Give the extent of all Plasmodium falciparum-infected red blood cells.
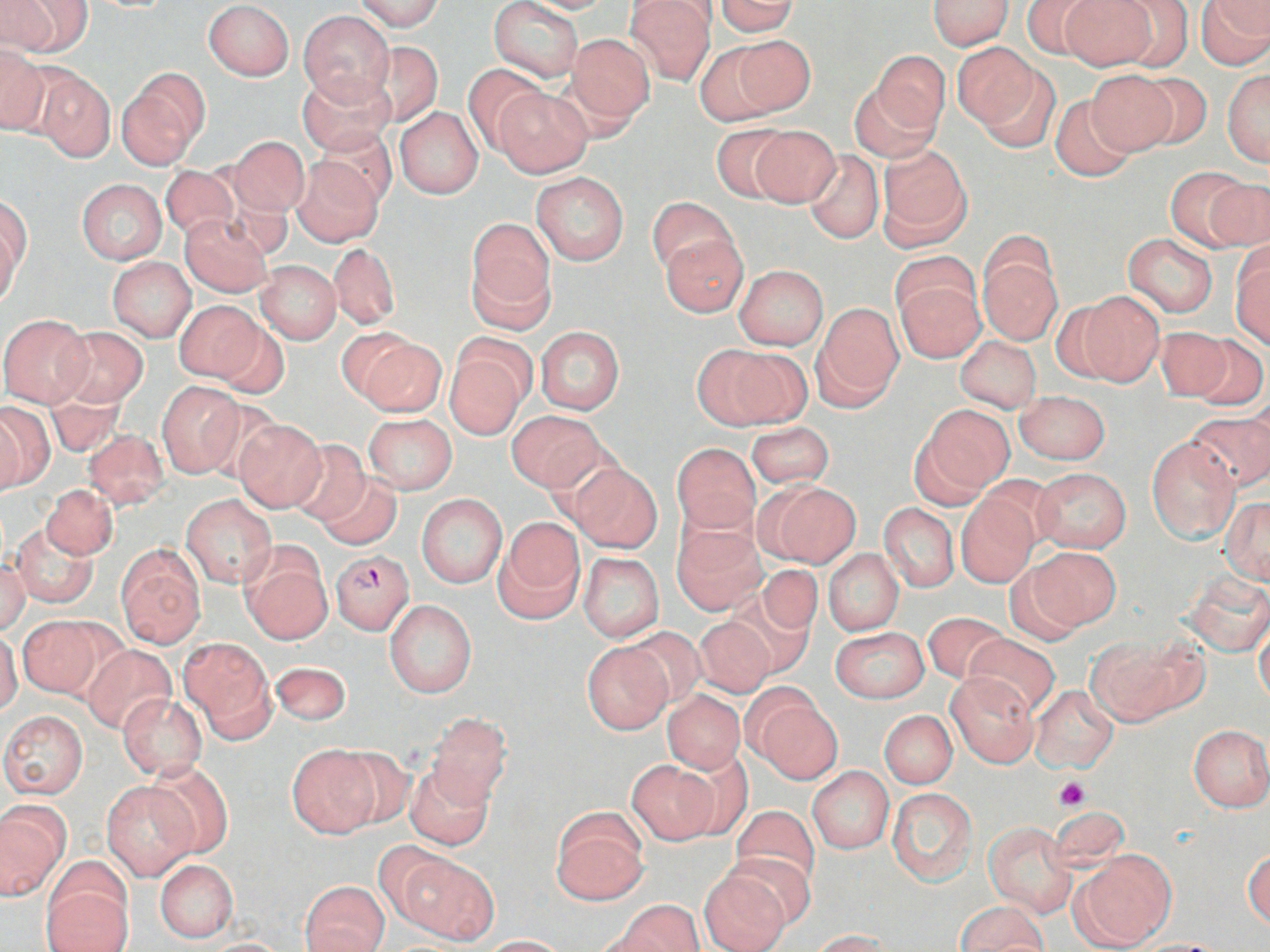
Approximate bounding boxes as (x1,y1)-(x2,y2) corner pairs in pixels.
Plasmodium falciparum-infected red blood cells: (330,551)-(414,634).

Summary:
  - Platelet locations: (1056,776)-(1089,810)
  - Uninfected red blood cell locations: (355,0)-(444,31), (515,0)-(620,15), (625,0)-(715,86), (714,0)-(801,35), (928,0)-(1013,50), (1019,0)-(1106,59), (1058,0)-(1158,71), (1107,0)-(1194,71), (1197,0)-(1270,68), (4,1)-(89,57), (202,1)-(294,79), (489,1)-(583,83), (297,10)-(395,105), (565,33)-(657,128), (727,35)-(816,116), (365,40)-(445,128), (952,42)-(1044,136), (0,44)-(49,135), (696,44)-(784,125), (872,51)-(950,134), (463,63)-(550,152), (977,65)-(1062,153), (34,68)-(114,162), (118,68)-(209,167), (1086,70)-(1178,154), (1223,70)-(1270,167), (298,71)-(397,154), (1132,73)-(1214,150), (852,79)-(941,161), (494,85)-(593,178), (1050,94)-(1138,182), (394,106)-(484,200), (709,123)-(796,200), (747,125)-(841,208), (314,126)-(397,208), (230,136)-(309,216), (876,142)-(972,250), (802,148)-(884,245), (292,157)-(384,246), (160,164)-(239,243), (1165,168)-(1257,251), (532,172)-(629,265), (1206,176)-(1270,251), (76,179)-(167,265), (1,198)-(30,296), (646,198)-(738,278), (180,214)-(274,296), (465,222)-(556,329), (1,226)-(21,309), (1122,233)-(1218,318), (658,234)-(749,316), (327,242)-(399,329), (1231,243)-(1270,347), (890,250)-(978,329), (978,250)-(1062,344), (107,257)-(196,341), (255,261)-(341,344), (734,265)-(828,350), (895,276)-(986,363), (1074,290)-(1165,387), (173,300)-(267,384), (812,303)-(904,409), (0,313)-(93,406), (208,318)-(290,400), (534,325)-(625,415), (57,326)-(148,407), (1154,326)-(1236,400), (353,332)-(446,417), (1190,333)-(1269,410), (955,336)-(1041,413), (443,345)-(530,442), (699,347)-(807,431), (157,381)-(244,477), (45,390)-(125,457), (1015,390)-(1111,465), (0,404)-(47,494), (922,405)-(1013,494), (506,410)-(606,491), (1187,410)-(1270,494), (362,413)-(458,494), (232,417)-(328,513), (747,423)-(835,488), (81,429)-(171,511), (1147,435)-(1241,544), (287,438)-(372,526), (672,442)-(760,533), (566,463)-(662,552), (1033,468)-(1132,553), (317,473)-(403,550), (767,482)-(860,566), (42,484)-(118,560), (957,492)-(1039,587), (417,494)-(507,588), (181,495)-(277,589), (1220,496)-(1270,584), (877,503)-(959,593), (495,519)-(584,621), (11,521)-(100,608), (672,523)-(767,614), (117,545)-(206,648), (1022,546)-(1120,632), (240,547)-(332,644), (824,550)-(903,635), (578,552)-(664,643), (0,560)-(32,634), (753,564)-(823,637), (1182,570)-(1270,655), (725,587)-(816,678), (385,599)-(477,698), (922,611)-(1011,684), (16,616)-(109,700), (693,618)-(777,697), (1255,620)-(1270,707), (622,625)-(708,712), (831,627)-(929,703), (0,630)-(22,716), (965,633)-(1059,717), (1085,635)-(1201,727), (181,640)-(275,739), (581,642)-(672,733), (82,644)-(177,734), (269,662)-(352,727), (945,671)-(1039,767), (1029,684)-(1119,772), (663,690)-(745,773), (117,693)-(207,780), (751,694)-(843,784), (0,710)-(88,799), (880,710)-(957,788), (426,713)-(512,809), (1187,724)-(1270,811), (286,744)-(381,838), (333,746)-(416,829), (674,753)-(753,840), (143,759)-(233,857), (626,759)-(719,844), (404,762)-(494,851), (807,767)-(895,853), (101,781)-(196,880), (887,787)-(977,885), (0,802)-(69,900), (731,805)-(820,894), (551,806)-(649,905), (984,820)-(1078,918), (373,841)-(463,932), (1072,848)-(1175,951), (1244,849)-(1270,929), (726,850)-(819,928), (395,853)-(501,945), (155,859)-(238,942), (698,867)-(791,952), (42,879)-(134,952), (301,881)-(389,952), (613,901)-(704,952), (954,901)-(1048,952), (811,929)-(892,952), (477,935)-(570,951), (198,938)-(295,951), (1131,939)-(1235,951)
  - Slide-level diagnosis: Plasmodium falciparum
  - Stain: May-Grünwald-Giemsa
  - Magnification: 1000x
  - Field of view: single
  - Preparation: thin blood film
  - Image size: 1270×952 pixels
  - Modality: optical microscopy